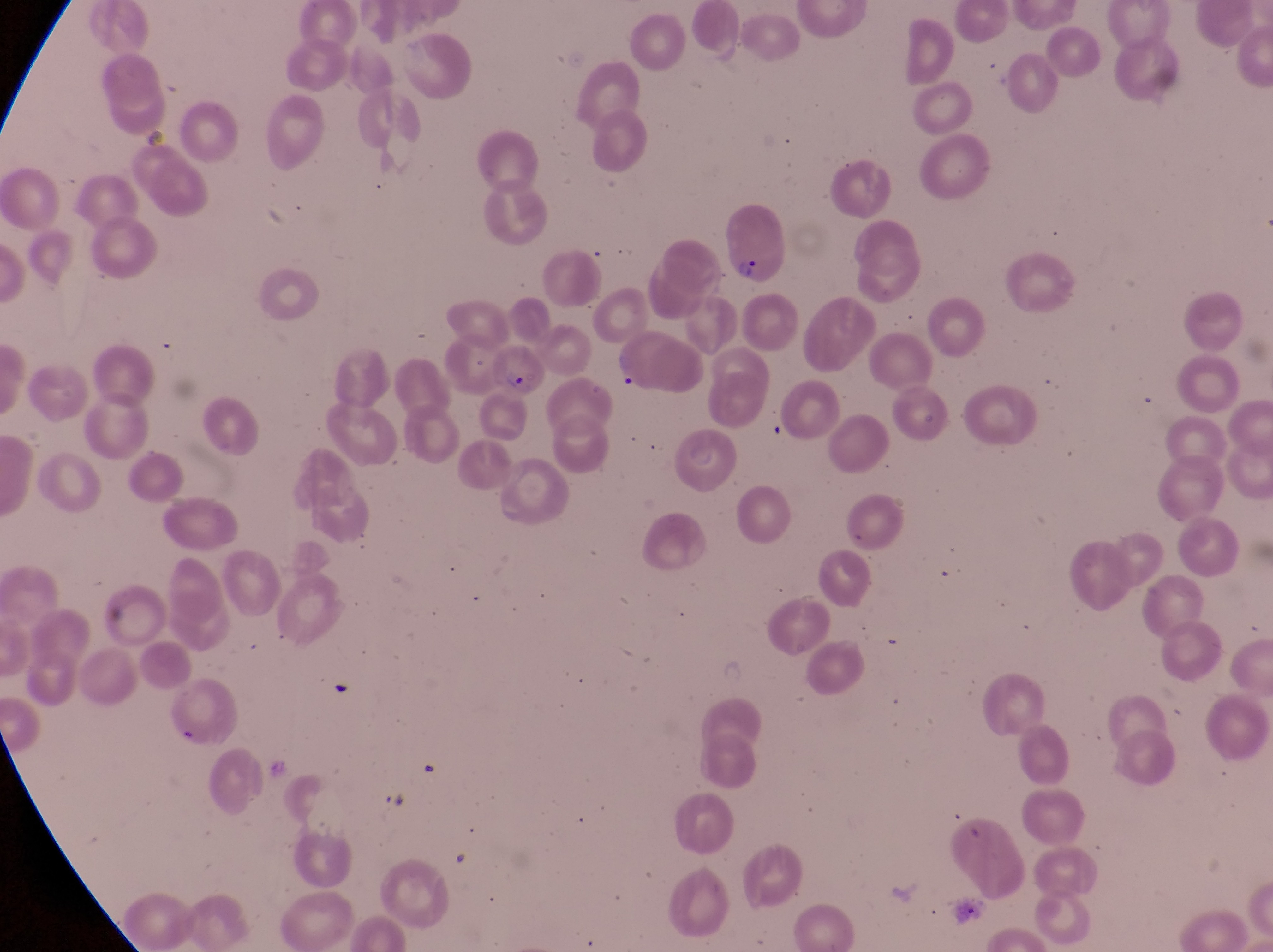
Approximate bounding boxes as [left, top, right, bottom] in pixels.
Summary:
  - Artifact (platelet-like body, stain precipitate, or debris) locations: [325, 677, 352, 705]
  - Parasitised red blood cell locations: [722, 204, 785, 286], [612, 332, 707, 399], [491, 345, 546, 400]
  - Magnification: 1000x
  - Country: Uganda
  - Capture: smartphone photograph through the eyepiece of an Olympus CX-23 microscope
  - Preparation: thin blood film
  - Image size: 1273×952 pixels
  - Field of view: single